Identify the parasite.
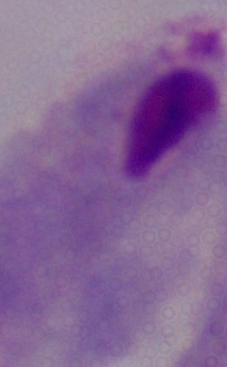
This is a trichomonad.

{
  "magnification": "1000x",
  "modality": "micrograph"
}